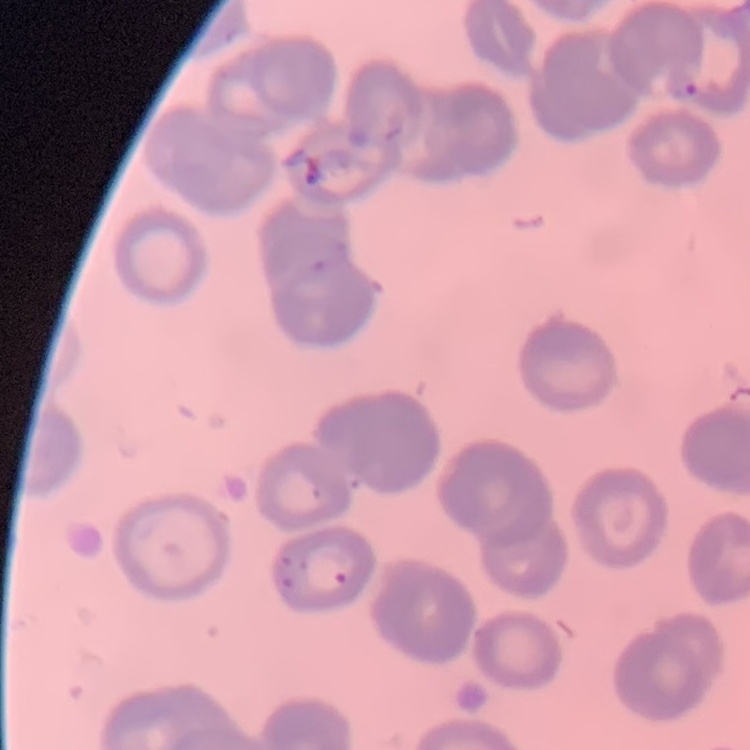
Summary:
  - Erythrocyte morphology: rouleaux formation
  - Image type: square crop of a larger photomicrograph
  - Stain: Field's or Giemsa
  - Preparation: thin blood film